Report the malaria status of this cell.
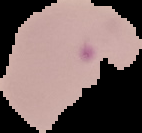
It is parasitized.

preparation = thin blood film
image size = 142×133 pixels
image type = segmented cell region with the area outside set to black